Evaluate for parasitized red blood cells.
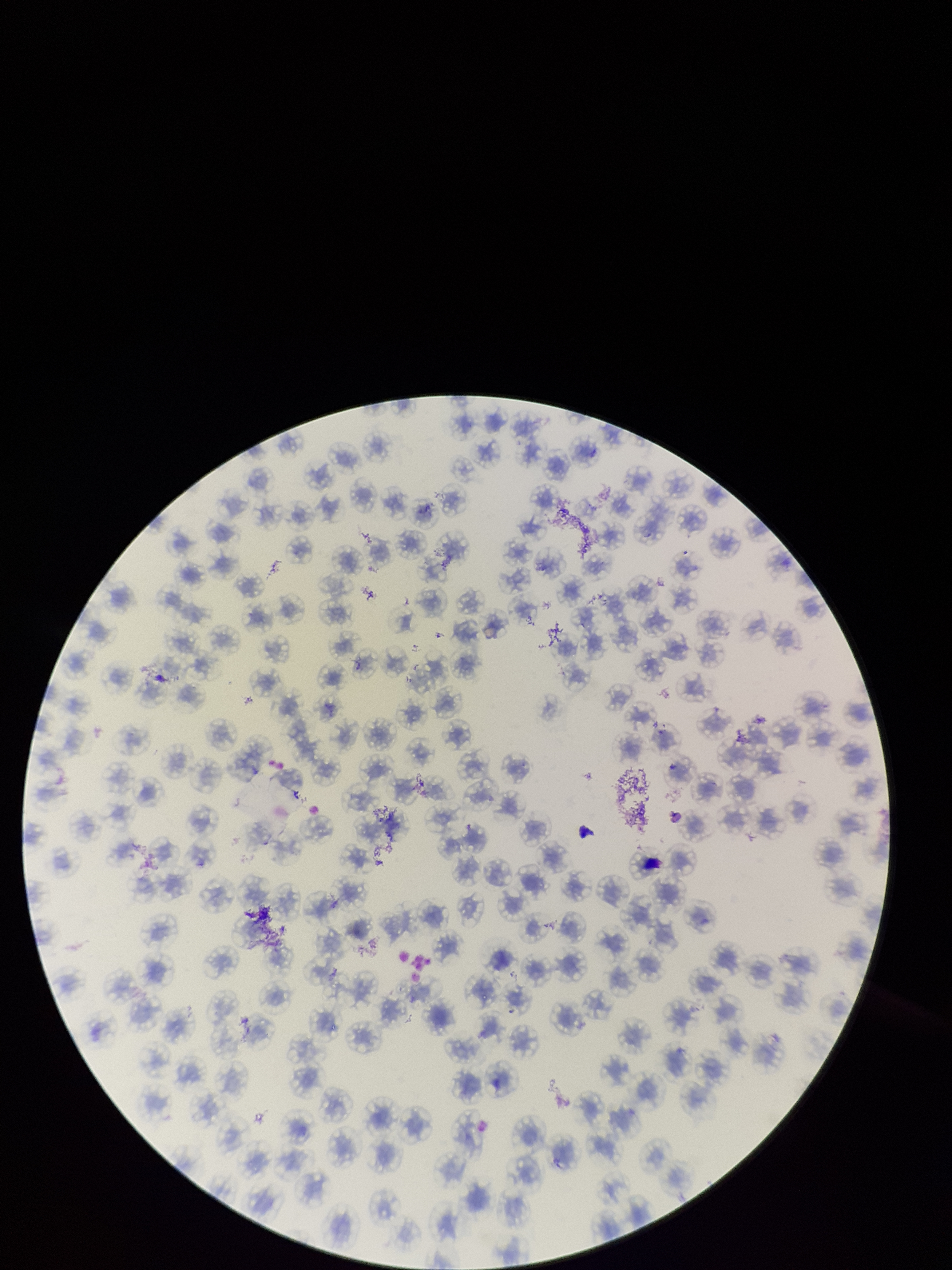

None detected.

Parasitized red blood cell count: 0. Patient malaria status: negative. Stained with Giemsa. One field from this slide. Red blood cell count: 138. Preparation: thin smear. Image is 952×1270 pixels. Photographed through the microscope eyepiece with a smartphone camera.